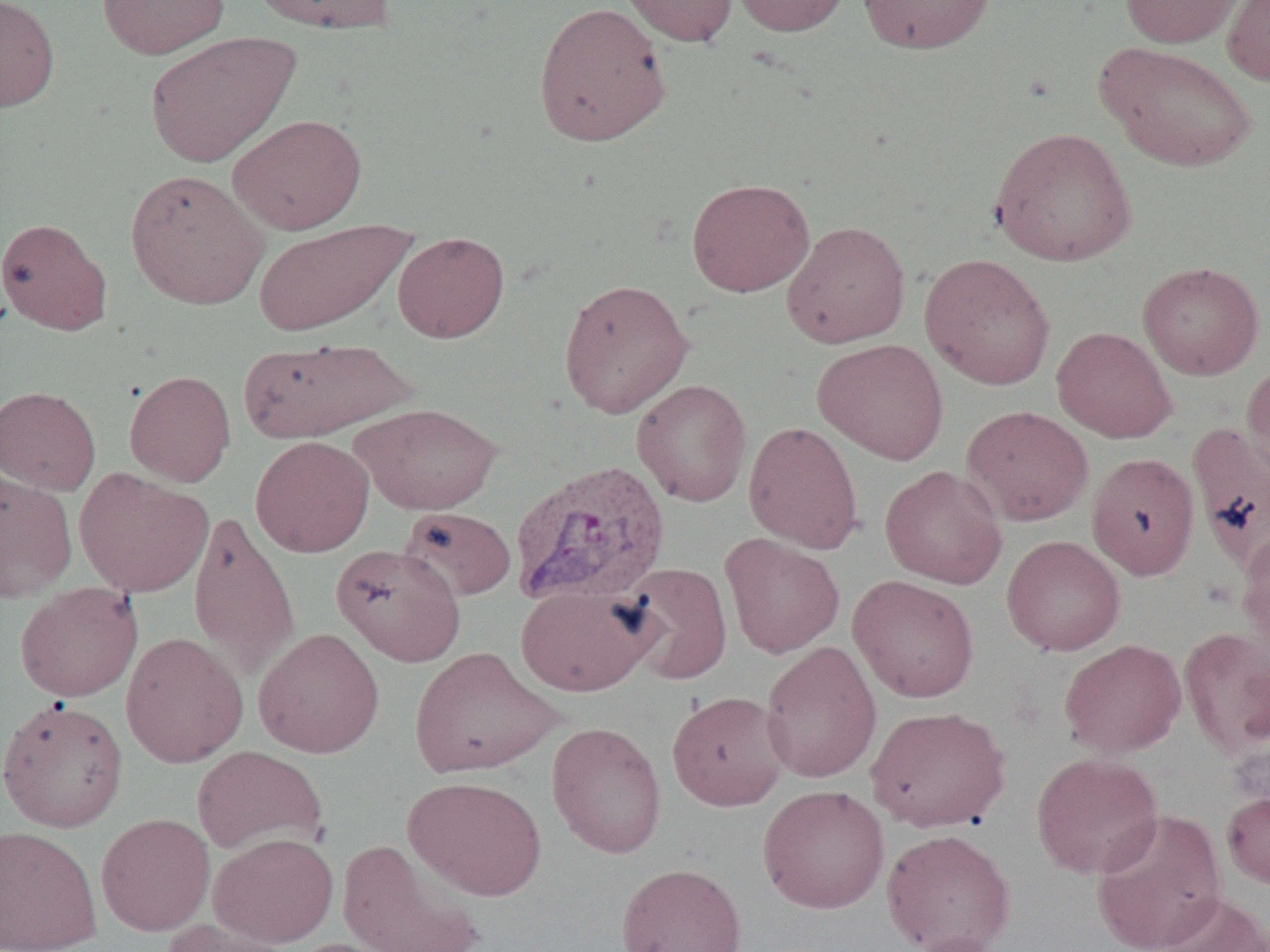
{
  "slide_level_diagnosis": "Plasmodium vivax",
  "uninfected_red_blood_cell_locations": "approximate bounding boxes as (x1,y1)-(x2,y2) corner pairs in pixels: (0,0)-(60,112), (97,0)-(230,59), (248,0)-(397,34), (618,0)-(738,47), (731,0)-(852,36), (856,0)-(997,54), (1119,0)-(1245,48), (1222,0)-(1270,86), (532,1)-(672,147), (144,31)-(301,168), (1096,41)-(1259,172), (228,113)-(367,234), (989,126)-(1137,267), (125,169)-(269,310), (686,177)-(815,297), (0,217)-(113,335), (253,218)-(417,337), (781,220)-(911,349), (393,231)-(510,343), (919,252)-(1056,390), (1137,261)-(1265,380), (557,278)-(694,418), (1052,326)-(1177,443), (238,336)-(416,444), (813,338)-(949,465), (1240,360)-(1270,486), (125,370)-(236,487), (631,379)-(752,507), (0,385)-(101,495), (350,402)-(503,514), (961,405)-(1093,526), (743,420)-(865,555), (1187,421)-(1270,577), (251,435)-(374,557), (1086,452)-(1200,581), (880,465)-(1007,589), (74,468)-(213,598), (0,470)-(78,602), (399,506)-(517,602), (188,509)-(300,683), (1236,526)-(1270,662), (720,533)-(845,658), (1001,535)-(1125,656), (331,543)-(466,666), (619,562)-(733,685), (848,574)-(980,703), (15,582)-(143,702), (515,584)-(658,697), (1178,626)-(1270,757), (253,627)-(385,758), (121,632)-(248,768), (1059,639)-(1186,758), (760,641)-(882,784), (409,646)-(562,779), (667,690)-(790,811), (0,697)-(129,833), (866,705)-(1011,832), (546,720)-(667,859), (191,745)-(328,856), (1031,751)-(1164,880), (403,775)-(548,901), (758,785)-(890,914), (1222,788)-(1270,890), (1090,808)-(1228,952), (95,812)-(215,936), (0,824)-(102,951), (881,827)-(1016,952), (209,832)-(339,948), (337,838)-(486,952), (616,861)-(747,952), (1153,891)-(1270,952), (158,918)-(297,952), (902,932)-(1011,952), (284,936)-(409,952)",
  "magnification": "1000x",
  "preparation": "thin blood smear",
  "field_of_view": "one of a larger specimen",
  "image_size": "1270×952 pixels",
  "modality": "light microscopy",
  "plasmodium_vivax_infected_red_blood_cell_locations": "approximate bounding boxes as (x1,y1)-(x2,y2) corner pairs in pixels: (509,459)-(670,607)"
}